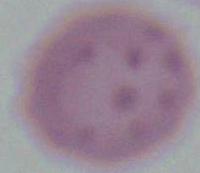
Summary:
  - Modality: photomicrograph
  - Magnification: 1000x
  - Identification: erythrocyte